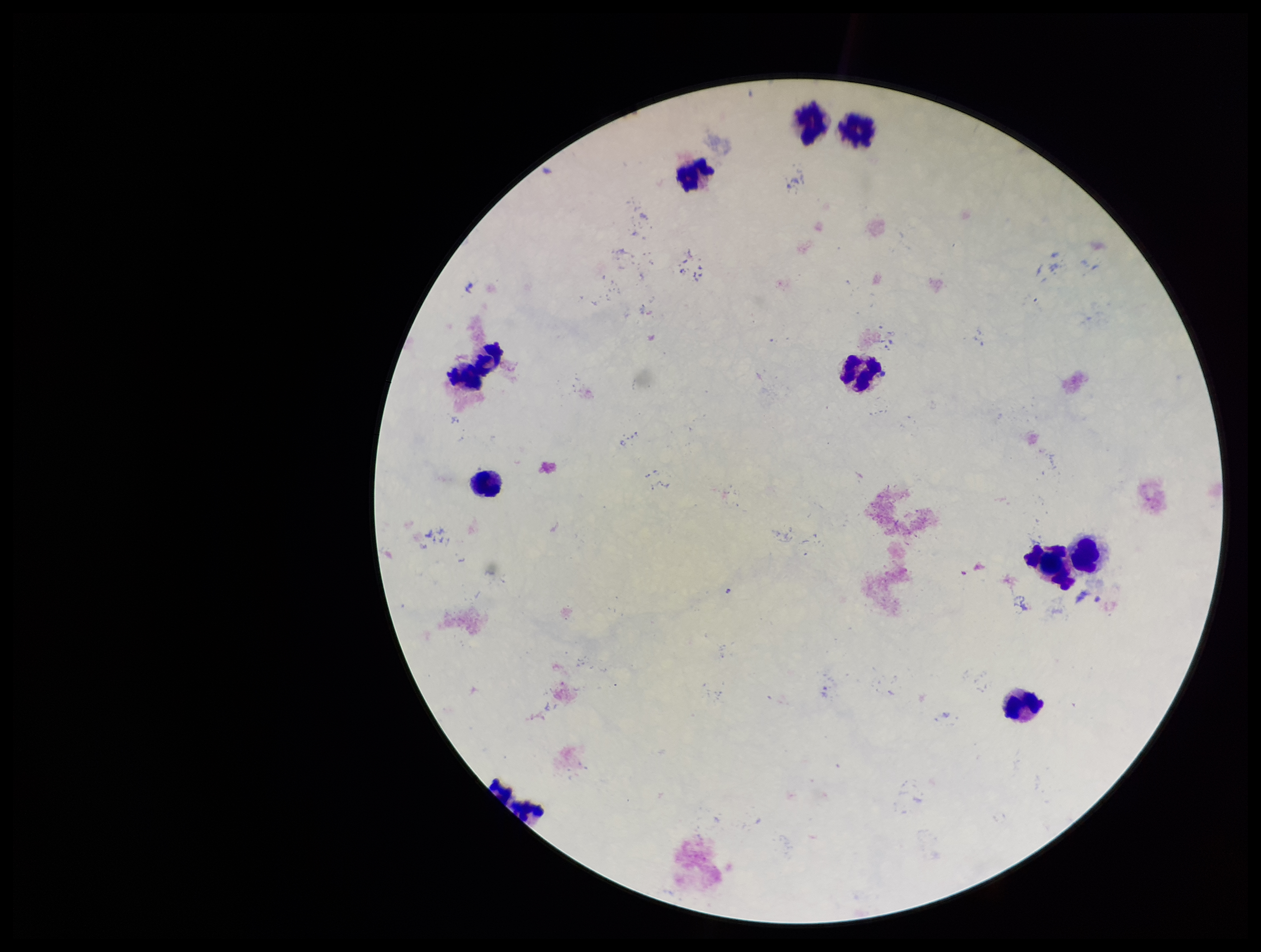
Parasite count: 0. Smartphone photograph taken through the eyepiece of a microscope. Patient malaria status: negative. Preparation: thick. One field from this slide. Image is 1261×952 pixels. Stained with Giemsa. Leukocyte count: 9. Plasmodium parasites: none seen.